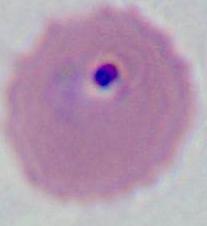 Captured at either 400x or 1000x magnification. Photomicrograph. A Plasmodium parasite is seen.